Report the malaria status of this cell.
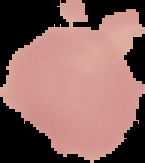
It is uninfected.

{
  "image_type": "segmented cell region on a black background",
  "image_size": "145×163 pixels",
  "preparation": "thin blood film"
}